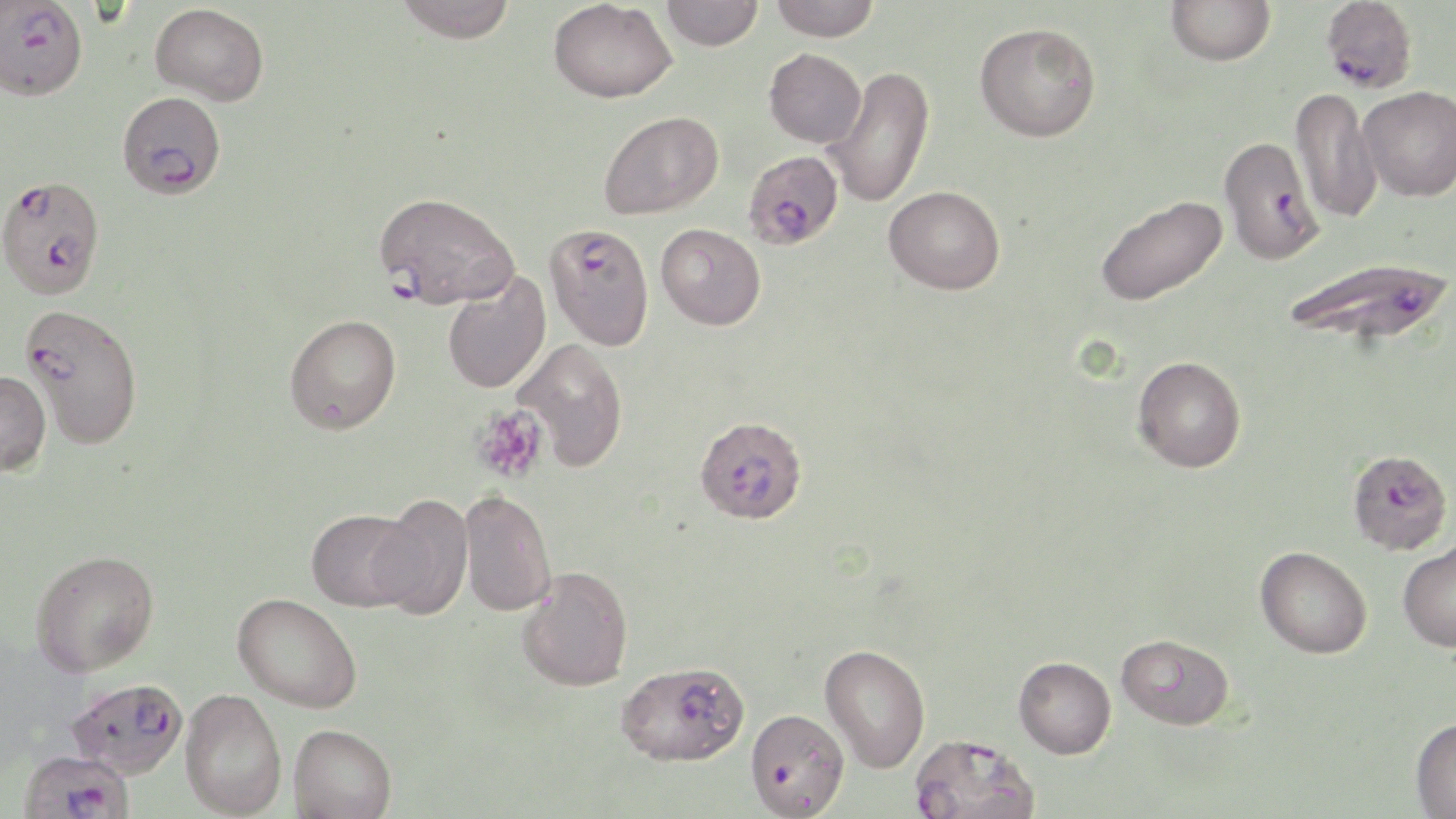
{
  "slide_level_diagnosis": "Plasmodium falciparum",
  "image_size": "1456×819 pixels",
  "field_of_view": "single",
  "uninfected_red_blood_cell_locations": "approximate bounding boxes as [x1, y1, x2, y2] in pixels: [393, 0, 517, 43], [661, 0, 762, 51], [768, 0, 880, 40], [1166, 0, 1276, 66], [548, 1, 677, 103], [150, 3, 269, 106], [974, 21, 1101, 142], [764, 48, 867, 147], [824, 66, 936, 209], [1359, 85, 1456, 201], [1290, 86, 1382, 225], [599, 110, 723, 219], [884, 185, 1005, 294], [1094, 195, 1228, 306], [656, 223, 766, 330], [441, 271, 551, 394], [284, 314, 401, 434], [512, 338, 629, 472], [1133, 355, 1246, 472], [0, 370, 51, 475], [458, 489, 556, 617], [369, 495, 473, 619], [306, 508, 419, 611], [1398, 539, 1456, 651], [1255, 545, 1372, 658], [31, 549, 159, 676], [517, 566, 633, 691], [233, 593, 362, 713], [1115, 633, 1235, 730], [819, 644, 930, 773], [1013, 656, 1116, 759], [180, 688, 287, 817], [1410, 716, 1456, 818], [289, 724, 396, 819]",
  "magnification": "1000x",
  "plasmodium_falciparum_infected_red_blood_cell_locations": "approximate bounding boxes as [x1, y1, x2, y2] in pixels: [1321, 0, 1418, 94], [1, 2, 88, 100], [117, 91, 226, 199], [1218, 135, 1325, 264], [742, 150, 845, 250], [0, 180, 99, 301], [373, 191, 520, 310], [544, 223, 654, 350], [1284, 256, 1453, 347], [20, 303, 144, 449], [694, 416, 807, 524], [1347, 448, 1452, 554], [615, 660, 749, 766], [67, 677, 189, 778], [745, 707, 849, 818], [908, 732, 1041, 819], [19, 748, 135, 819]",
  "platelet_locations": "approximate bounding boxes as [x1, y1, x2, y2] in pixels: [470, 404, 548, 483]",
  "modality": "optical microscopy",
  "stain": "May-Grünwald-Giemsa",
  "preparation": "thin blood film"
}